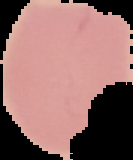
image_size: 133×160 pixels
result: no malaria parasites seen
image_type: segmented cell region with the area outside set to black
preparation: thin blood smear